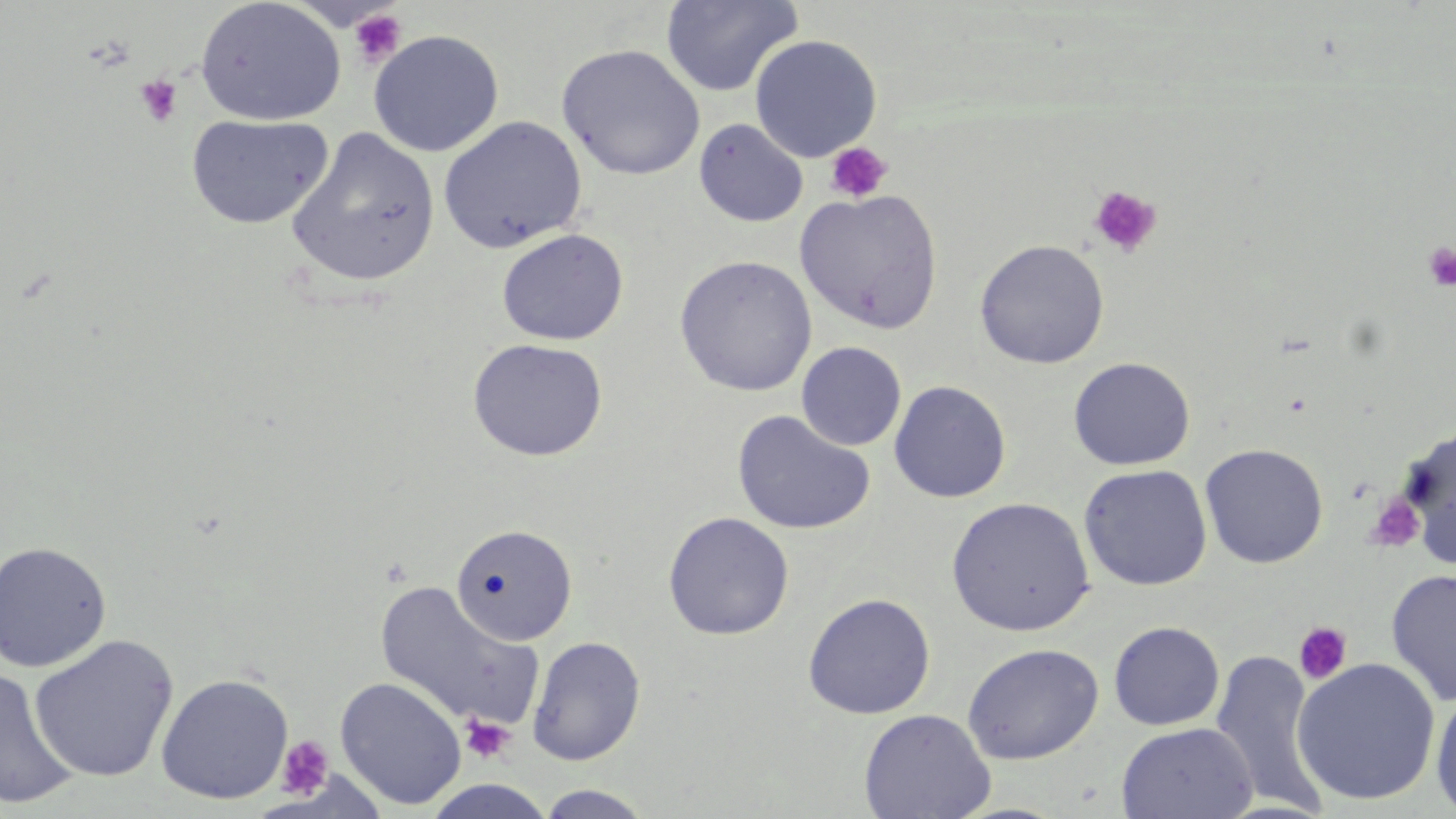

slide_level_diagnosis: no evidence of blood parasites
image_size: 1456×819 pixels
modality: optical microscopy
field_of_view: single
platelet_locations: 'approximate bounding boxes as (x1, y1, x2, y2) in pixels: (348, 8, 407, 68), (134, 74, 183, 128), (825, 142, 892, 203), (1089, 185, 1162, 258), (1421, 242, 1456, 291), (1365, 493, 1426, 552), (1293, 621, 1353, 685), (460, 714, 516, 764), (275, 735, 335, 799)'
magnification: 1000x
uninfected_red_blood_cell_locations: 'approximate bounding boxes as (x1, y1, x2, y2) in pixels: (194, 0, 346, 127), (661, 0, 802, 97), (367, 29, 504, 157), (749, 34, 883, 162), (557, 43, 706, 181), (185, 113, 333, 229), (438, 115, 588, 253), (694, 118, 808, 227), (287, 126, 441, 288), (794, 189, 945, 333), (495, 228, 629, 345), (973, 239, 1110, 369), (674, 254, 817, 397), (467, 337, 608, 461), (797, 341, 907, 450), (1068, 356, 1195, 470), (888, 379, 1012, 503), (732, 409, 876, 535), (1398, 425, 1456, 560), (1199, 442, 1329, 568), (1078, 463, 1213, 591), (946, 497, 1096, 637), (662, 511, 794, 640), (450, 523, 577, 647), (0, 542, 112, 672), (1385, 567, 1456, 707), (374, 581, 545, 732), (802, 592, 936, 719), (1108, 621, 1225, 731), (29, 633, 179, 783), (527, 635, 646, 766), (962, 643, 1104, 764), (1208, 649, 1331, 813), (1291, 657, 1441, 806), (0, 664, 81, 811), (155, 673, 294, 804), (334, 676, 467, 809), (1430, 689, 1456, 818), (858, 708, 995, 819), (1116, 721, 1258, 819), (534, 785, 657, 818)'
stain: May-Grünwald-Giemsa
preparation: thin blood smear